Assess this cell for malaria.
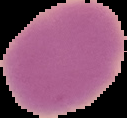
Uninfected.

{
  "preparation": "thin blood smear",
  "image_type": "segmented cell region with the area outside set to black",
  "image_size": "127×118 pixels"
}